Assess the morphology of the erythrocytes.
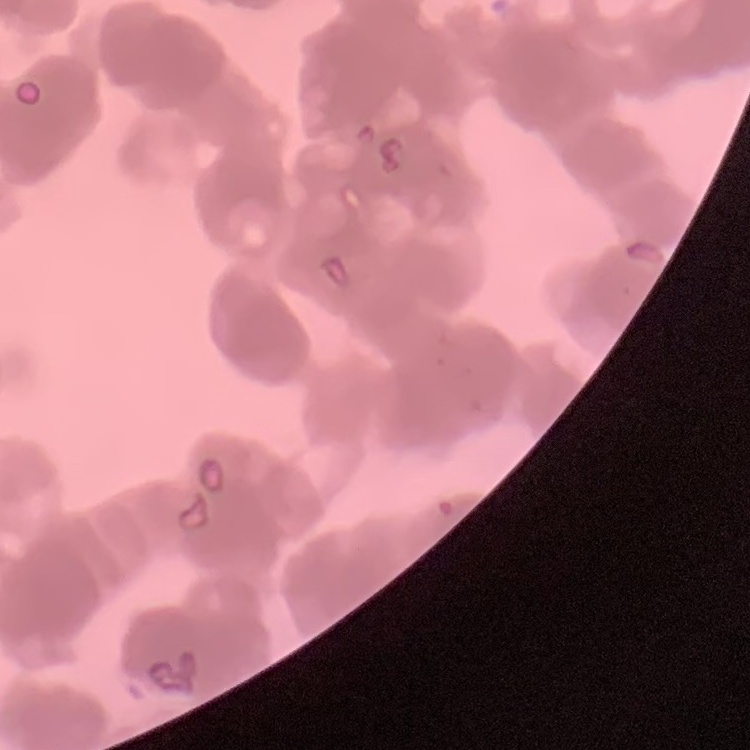
They show rouleaux formation.

Field's or Giemsa stain. One tile cut from a larger photomicrograph. Thin blood film.